Report the malaria status of this cell.
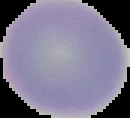
It is uninfected.

Summary:
  - Image type: segmented cell region on a black background
  - Image size: 130×118 pixels
  - Preparation: thin blood film